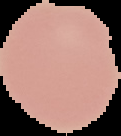

Image is 121×136 pixels. Segmented cell region on a black background. Malaria status: uninfected. From a thin blood smear.